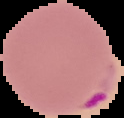
Summary:
  - Preparation: thin blood film
  - Image size: 124×118 pixels
  - Image type: segmented cell region on a black background
  - Malaria status: parasitized